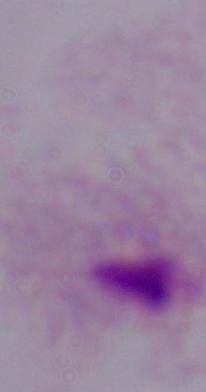

Summary:
  - Identification: trichomonad
  - Modality: micrograph
  - Magnification: 1000x